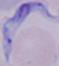

Photomicrograph. A trypanosome is seen. 1000x magnification.